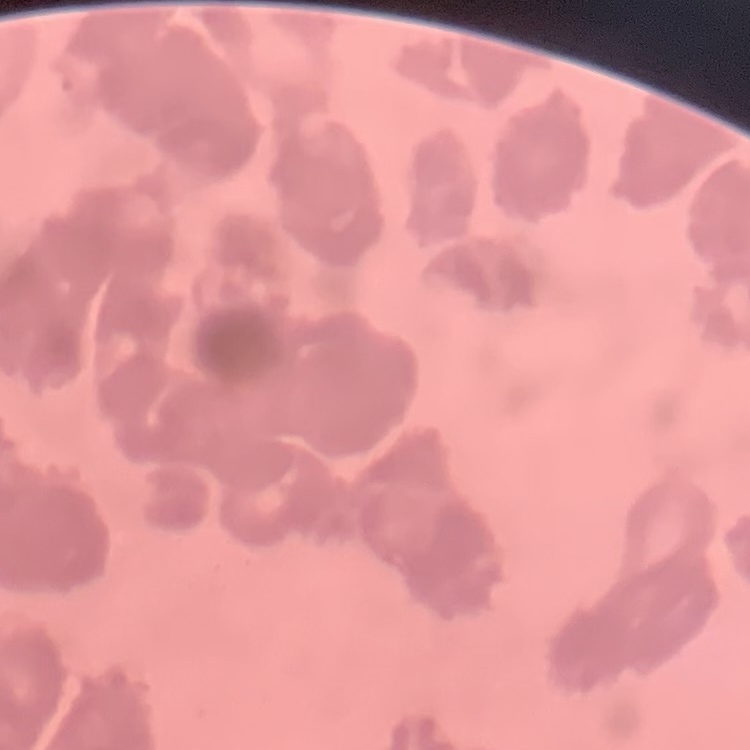
erythrocyte morphology = rouleaux formation
stain = Field's or Giemsa
image type = one tile cut from a larger photomicrograph
preparation = thin blood smear